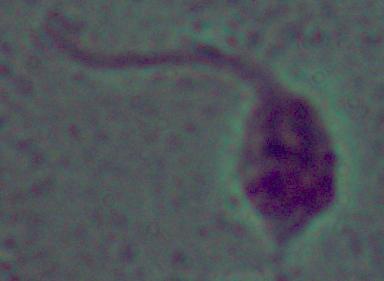

identification = Leishmania
modality = micrograph
magnification = 1000x